Identify the cell.
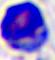

A leukocyte.

Summary:
  - Modality: micrograph
  - Magnification: 400x